Outline each uninfected red blood cell.
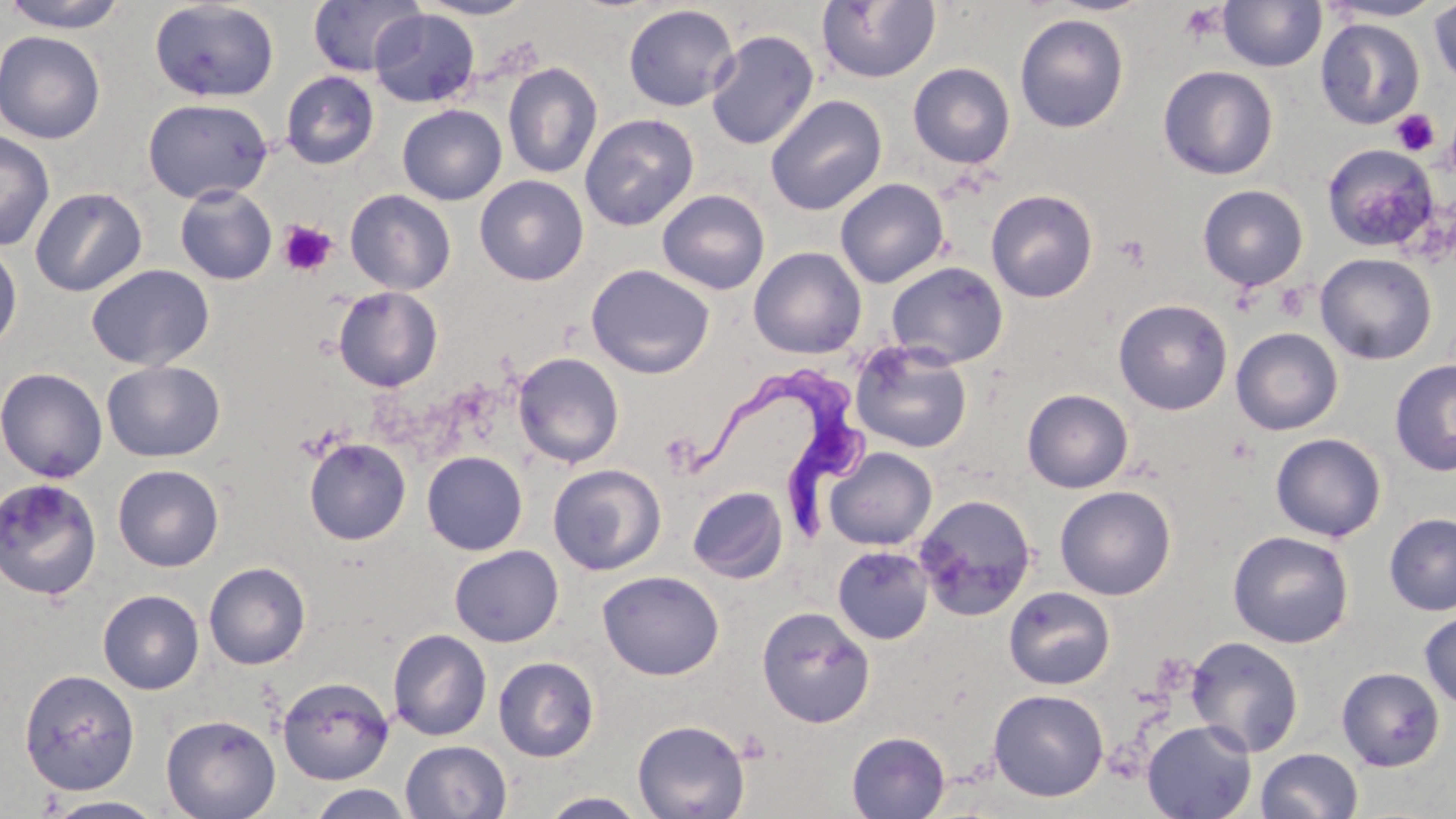
Approximate bounding boxes as (x1, y1, x2, y2) in pixels.
Uninfected red blood cells: (0, 0, 135, 33), (307, 0, 425, 77), (414, 0, 537, 20), (1217, 0, 1326, 72), (1318, 0, 1449, 23), (149, 1, 279, 103), (816, 1, 942, 84), (1428, 1, 1456, 88), (623, 4, 739, 112), (369, 8, 480, 108), (1014, 13, 1129, 133), (1314, 18, 1426, 130), (705, 29, 819, 150), (0, 30, 106, 144), (502, 62, 603, 179), (908, 62, 1015, 168), (1158, 64, 1279, 180), (281, 71, 379, 169), (765, 94, 887, 216), (142, 98, 273, 204), (397, 104, 507, 205), (579, 113, 699, 231), (0, 130, 55, 251), (1322, 143, 1440, 253), (474, 175, 589, 286), (834, 178, 949, 288), (174, 184, 278, 285), (1197, 184, 1308, 291), (29, 186, 148, 297), (345, 189, 456, 295), (657, 189, 770, 295), (986, 189, 1098, 303), (0, 239, 23, 355), (748, 247, 867, 359), (1315, 252, 1437, 364), (886, 261, 1009, 368), (86, 264, 215, 371), (586, 264, 715, 379), (861, 273, 991, 422), (333, 286, 443, 392), (1113, 298, 1233, 415), (1230, 327, 1343, 435), (850, 340, 973, 454), (512, 352, 625, 468), (1389, 358, 1456, 477), (101, 359, 225, 462), (0, 367, 108, 482), (1022, 389, 1133, 493), (1270, 432, 1386, 542), (304, 438, 411, 545), (824, 447, 937, 550), (421, 451, 528, 555), (113, 464, 224, 572), (547, 464, 666, 575), (0, 477, 102, 601), (1054, 485, 1176, 601), (687, 486, 789, 583), (913, 494, 1038, 620), (1384, 512, 1456, 616), (1228, 530, 1354, 648), (449, 545, 563, 647), (832, 545, 934, 645), (203, 562, 311, 670), (597, 570, 725, 680), (1003, 586, 1116, 690), (97, 589, 205, 694), (757, 606, 875, 727), (1419, 611, 1456, 708), (388, 628, 492, 741), (1185, 635, 1305, 756), (493, 656, 600, 762), (1336, 667, 1445, 771), (18, 668, 141, 795), (277, 676, 395, 785), (988, 688, 1109, 801), (161, 713, 281, 819), (632, 719, 750, 819), (1141, 720, 1257, 819), (846, 731, 950, 818), (400, 740, 512, 819), (1255, 748, 1364, 819), (306, 784, 414, 818), (539, 791, 650, 818), (42, 796, 168, 818).

Trypanosoma brucei locations: (690, 376, 877, 544). Platelet locations: (1177, 3, 1227, 45), (1391, 109, 1439, 157), (278, 220, 337, 277), (1113, 234, 1151, 270), (1273, 282, 1311, 322). Slide-level diagnosis: Trypanosoma brucei. Thin blood smear. Image is 1456×819 pixels. Captured at 1000x magnification. Single field of view. Optical microscopy. May-Grünwald-Giemsa stain.